Give the preparation type.
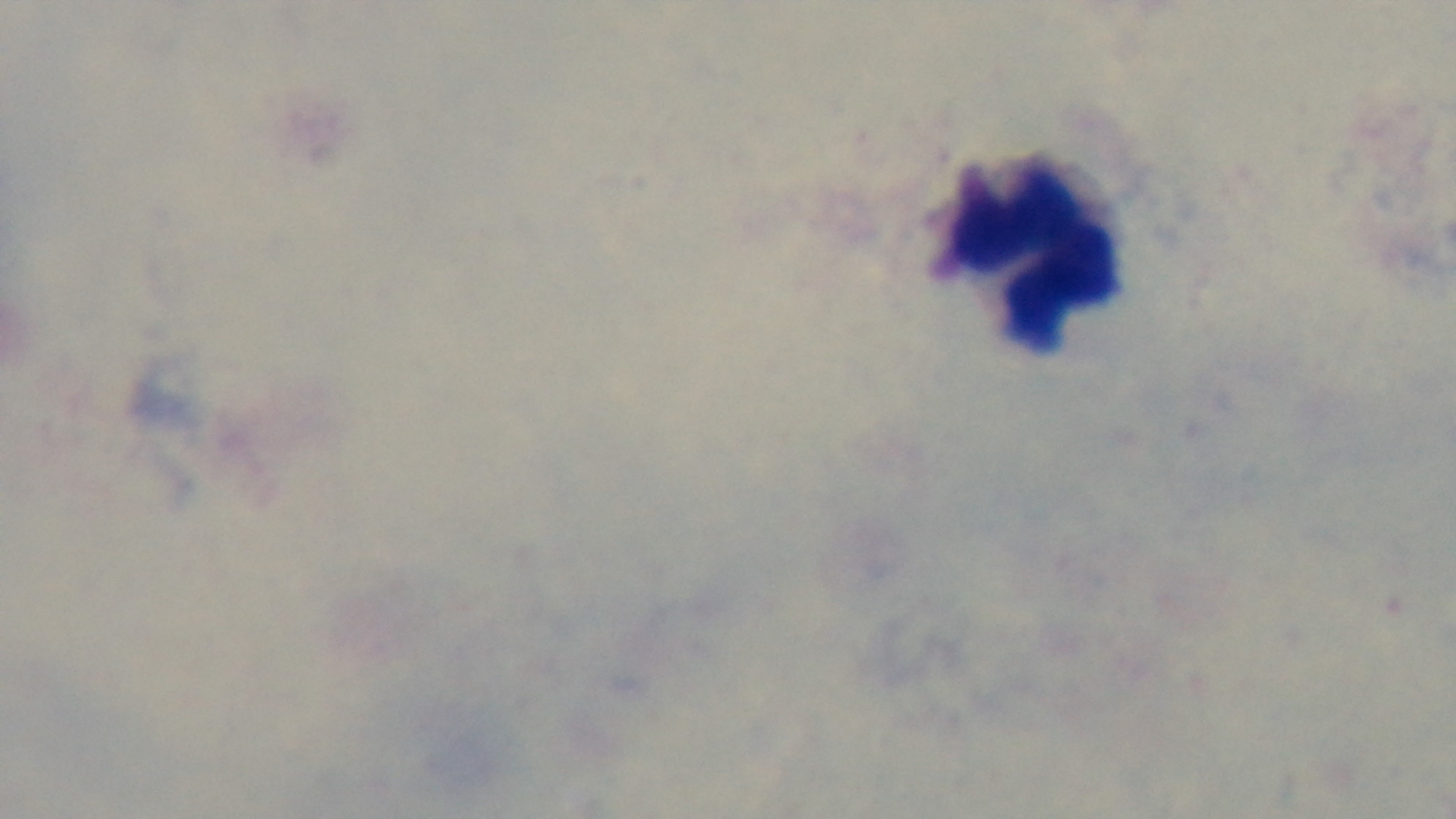
A thick smear.

field of view = single
capture = mounted 4K digital camera
stain = Giemsa
modality = light microscopy
malaria status = negative
objective = 100x oil immersion